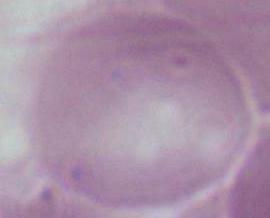

Captured at 1000x magnification. Micrograph. A red blood cell is shown.